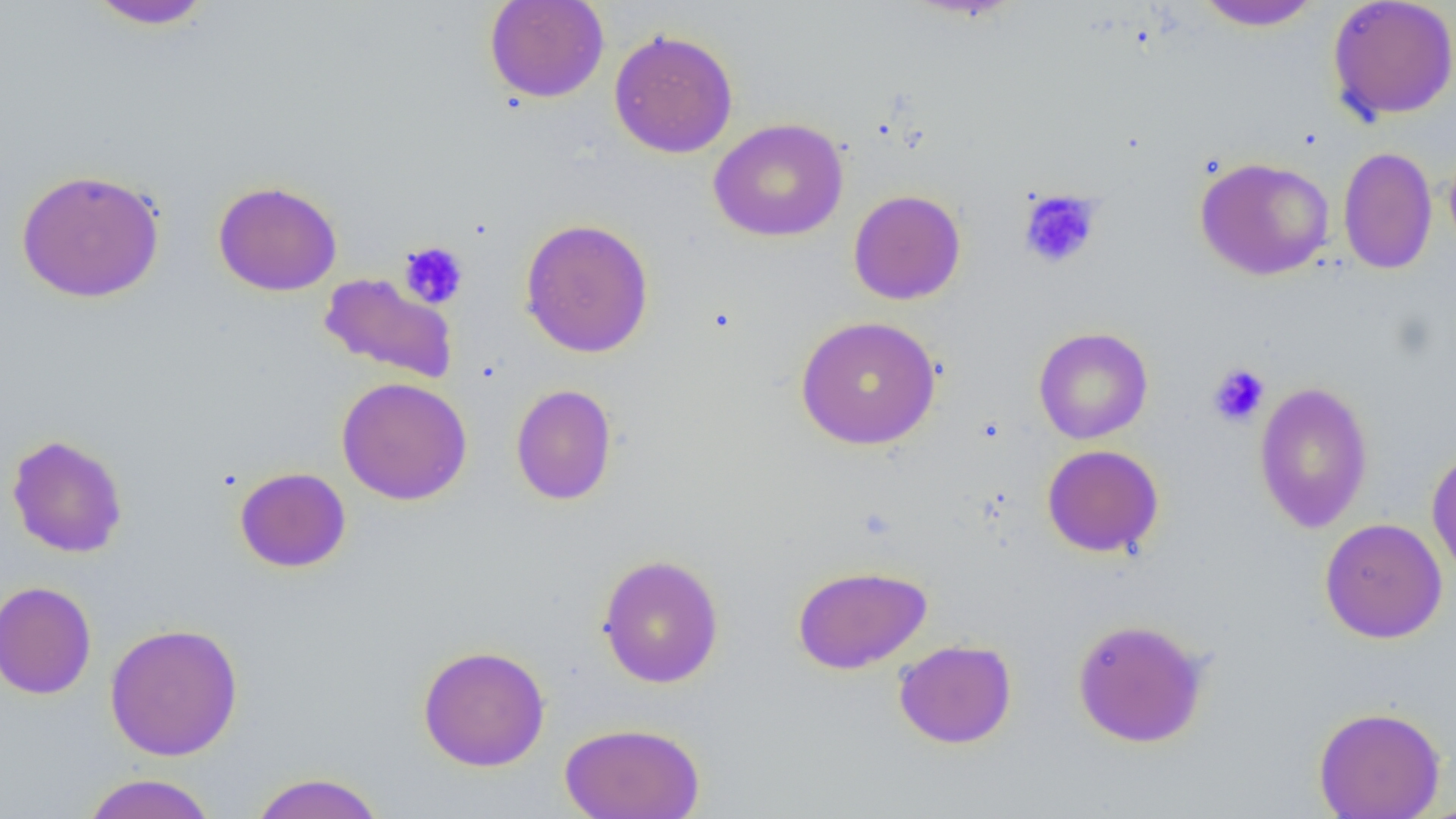 Approximate bounding boxes as [x1, y1, x2, y2] in pixels. Platelet locations: [1018, 189, 1103, 270], [398, 241, 468, 309], [1207, 362, 1271, 428]. Uninfected red blood cell locations: [83, 0, 216, 30], [484, 0, 609, 103], [1194, 0, 1321, 31], [1327, 1, 1456, 122], [609, 28, 739, 159], [708, 119, 849, 242], [1337, 146, 1438, 275], [1194, 156, 1334, 280], [15, 168, 166, 303], [212, 180, 342, 296], [848, 189, 966, 305], [518, 217, 655, 358], [318, 273, 458, 384], [795, 314, 941, 450], [1033, 326, 1153, 444], [336, 377, 472, 505], [1253, 382, 1374, 533], [510, 384, 617, 505], [6, 433, 128, 559], [1042, 444, 1164, 557], [1426, 448, 1456, 579], [234, 467, 351, 573], [1320, 517, 1448, 643], [597, 553, 724, 689], [792, 564, 932, 674], [0, 580, 97, 699], [1071, 617, 1210, 748], [104, 622, 244, 761], [893, 639, 1017, 749], [417, 644, 551, 771], [1313, 706, 1446, 818], [559, 722, 706, 819], [80, 772, 220, 818], [249, 772, 387, 819]. Slide-level diagnosis: negative for blood parasites. Light microscopy. Image is 1456×819 pixels. Captured at 1000x magnification. Thin blood film. Single field of view.